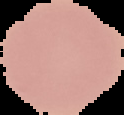
image size = 124×115 pixels
malaria status = uninfected
preparation = thin blood film
image type = segmented cell region with the area outside set to black